Assess this cell for malaria.
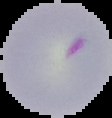

Parasitized.

image_type: cell region segmented out of the field of view; surrounding area masked to black
image_size: 112×118 pixels
preparation: thin blood smear